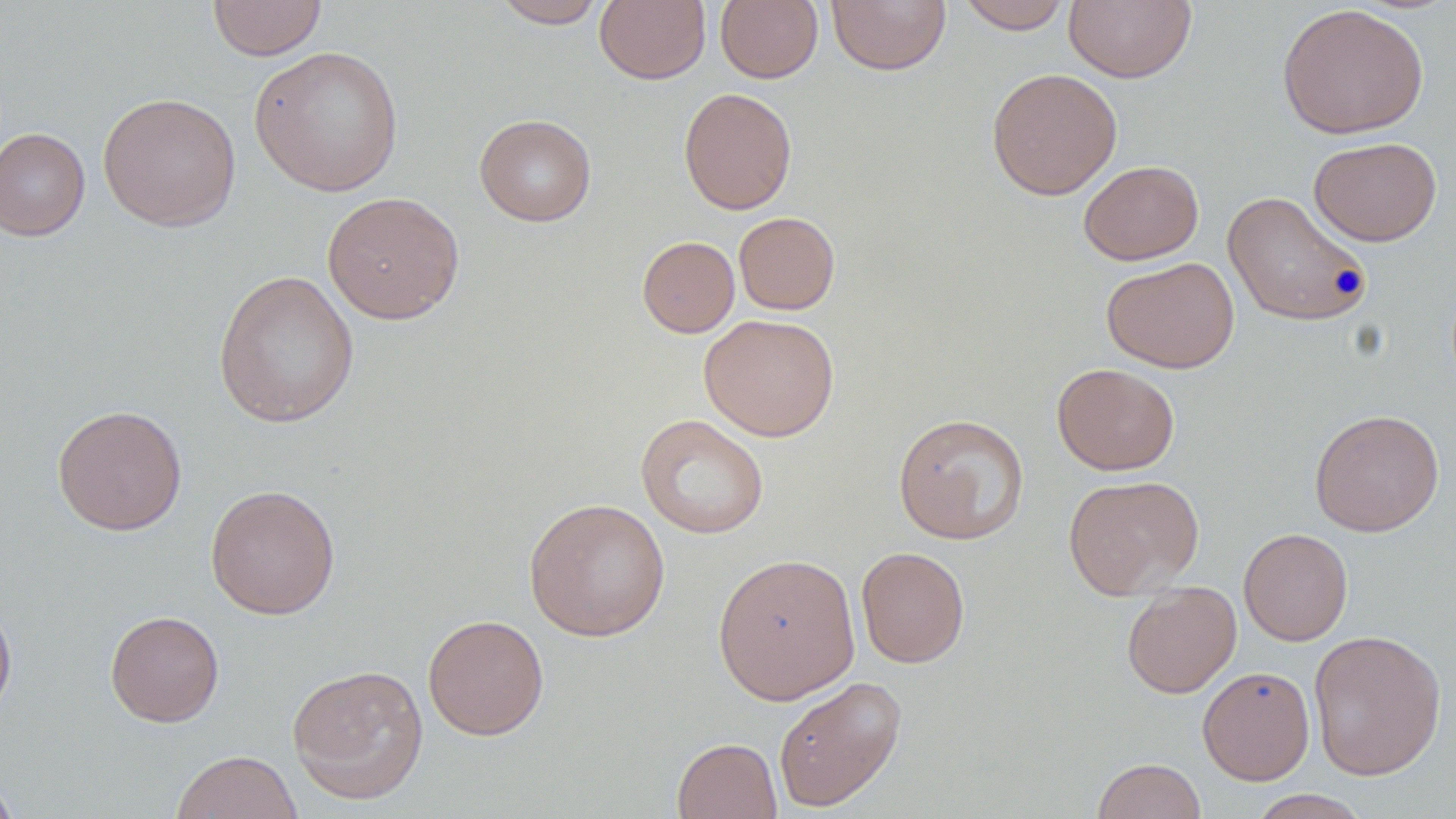
slide-level diagnosis = negative for blood parasites
uninfected red blood cell locations = approximate bounding boxes as [x1, y1, x2, y2] in pixels: [207, 0, 326, 60], [491, 0, 608, 28], [594, 0, 710, 85], [715, 0, 823, 83], [955, 0, 1074, 34], [1065, 0, 1196, 83], [826, 1, 951, 75], [1276, 3, 1429, 140], [249, 45, 404, 197], [986, 67, 1123, 200], [678, 87, 798, 215], [98, 91, 241, 232], [474, 113, 597, 226], [0, 126, 91, 241], [1308, 136, 1442, 246], [1078, 160, 1204, 265], [1222, 190, 1373, 327], [321, 191, 465, 325], [734, 212, 840, 315], [637, 235, 740, 338], [1101, 256, 1240, 373], [212, 269, 360, 428], [699, 313, 839, 441], [1051, 362, 1180, 476], [51, 404, 187, 535], [1308, 409, 1445, 536], [893, 412, 1030, 545], [636, 414, 769, 539], [1062, 474, 1204, 599], [204, 483, 341, 619], [523, 496, 670, 642], [1238, 527, 1353, 645], [856, 546, 970, 668], [712, 552, 861, 704], [1121, 581, 1241, 698], [0, 597, 17, 725], [105, 610, 224, 727], [423, 613, 549, 740], [1308, 629, 1447, 781], [286, 663, 429, 804], [1197, 665, 1315, 785], [772, 675, 907, 812], [672, 737, 782, 819], [170, 750, 303, 819], [1091, 757, 1207, 819], [0, 768, 20, 818], [1247, 789, 1372, 818]
preparation = thin blood film
field of view = single
image size = 1456×819 pixels
stain = May-Grünwald-Giemsa
modality = light microscopy
magnification = 1000x